Identify the blood parasite species.
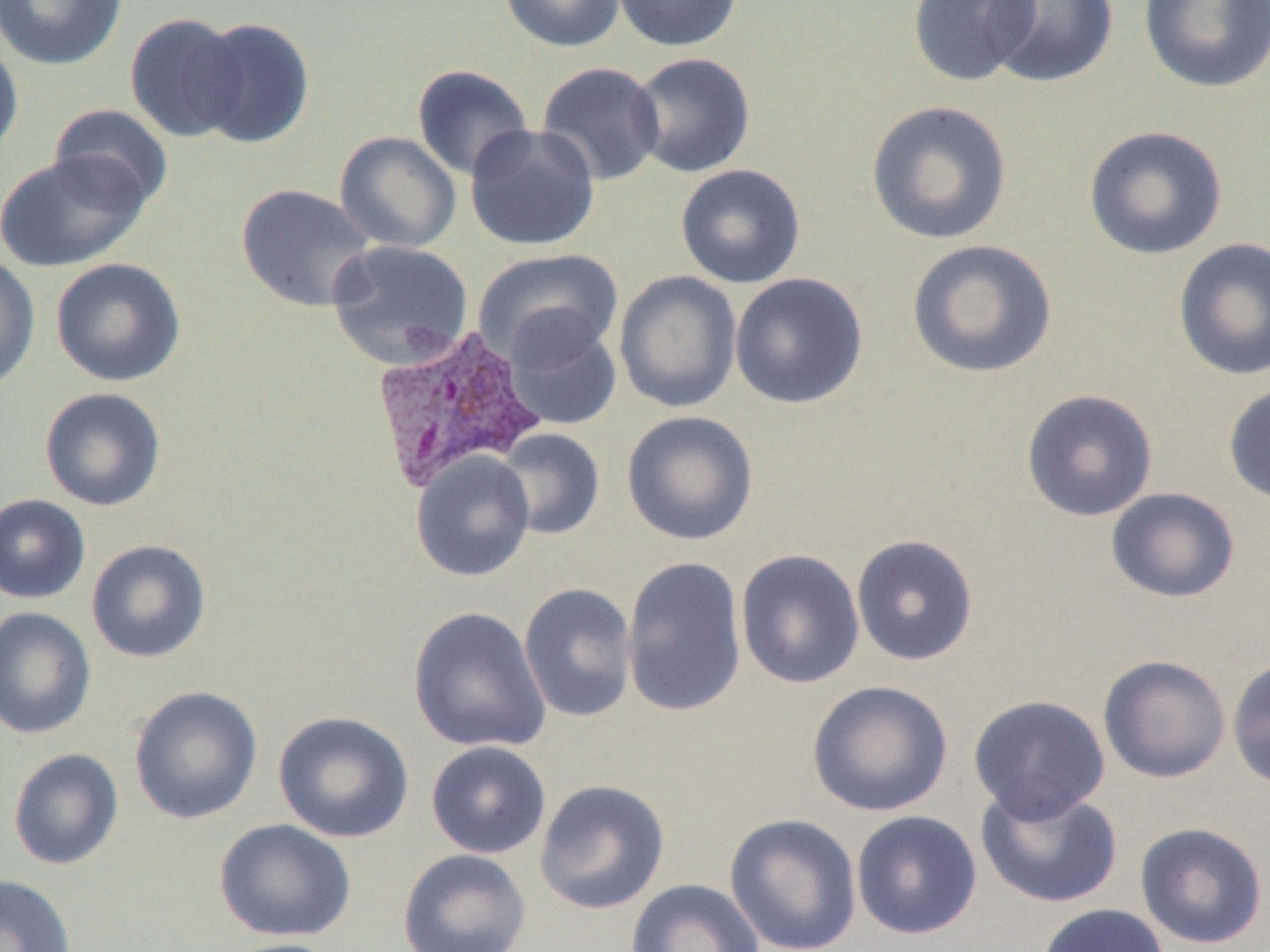

Plasmodium vivax.

Approximate bounding boxes as (x1, y1, x2, y2) in pixels. Uninfected red blood cell locations: (0, 0, 127, 70), (499, 0, 625, 53), (611, 0, 743, 52), (907, 0, 1040, 86), (986, 0, 1119, 87), (1138, 0, 1270, 93), (125, 12, 249, 143), (190, 16, 315, 149), (0, 37, 23, 163), (628, 52, 756, 178), (536, 62, 666, 186), (412, 64, 534, 180), (866, 99, 1013, 245), (49, 104, 173, 214), (465, 123, 601, 252), (1083, 125, 1227, 260), (334, 131, 462, 253), (0, 151, 148, 272), (675, 164, 806, 289), (236, 183, 376, 313), (1172, 237, 1270, 381), (906, 239, 1057, 379), (327, 240, 474, 369), (473, 248, 623, 368), (0, 253, 40, 393), (50, 257, 186, 387), (614, 270, 742, 413), (729, 272, 869, 409), (503, 314, 622, 431), (1223, 382, 1270, 507), (39, 387, 167, 511), (1020, 388, 1158, 522), (621, 410, 759, 546), (494, 428, 605, 541), (410, 450, 536, 582), (1105, 487, 1240, 603), (0, 493, 90, 604), (851, 533, 979, 666), (86, 539, 212, 663), (735, 549, 866, 689), (621, 556, 747, 718), (518, 582, 638, 723), (408, 606, 551, 753), (0, 607, 96, 739), (1097, 654, 1231, 783), (1226, 656, 1270, 790), (806, 679, 954, 817), (129, 685, 263, 824), (968, 695, 1110, 822), (273, 710, 414, 843), (426, 741, 551, 859), (8, 748, 124, 870), (535, 779, 670, 914), (976, 784, 1123, 908), (851, 809, 982, 940), (724, 813, 863, 952), (214, 818, 357, 941), (1134, 821, 1269, 949), (397, 848, 532, 952), (0, 875, 76, 952), (626, 879, 765, 952), (1037, 903, 1170, 952), (217, 938, 347, 952). Plasmodium vivax-infected red blood cell locations: (370, 326, 547, 493). Image is 1270×952 pixels. Thin blood smear. 1000x magnification. Light microscopy. Single field of view.